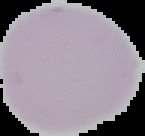
From a thin blood film. Result: negative for malaria parasites. Cell region segmented out of the field of view; the surrounding area is masked to black. Image is 145×136 pixels.